Classify this cell by malaria status.
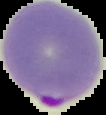

It is parasitized.

From a thin blood film. The area outside the segmented cell region is set to black. Image is 106×115 pixels.